Locate every Plasmodium parasite and every leukocyte.
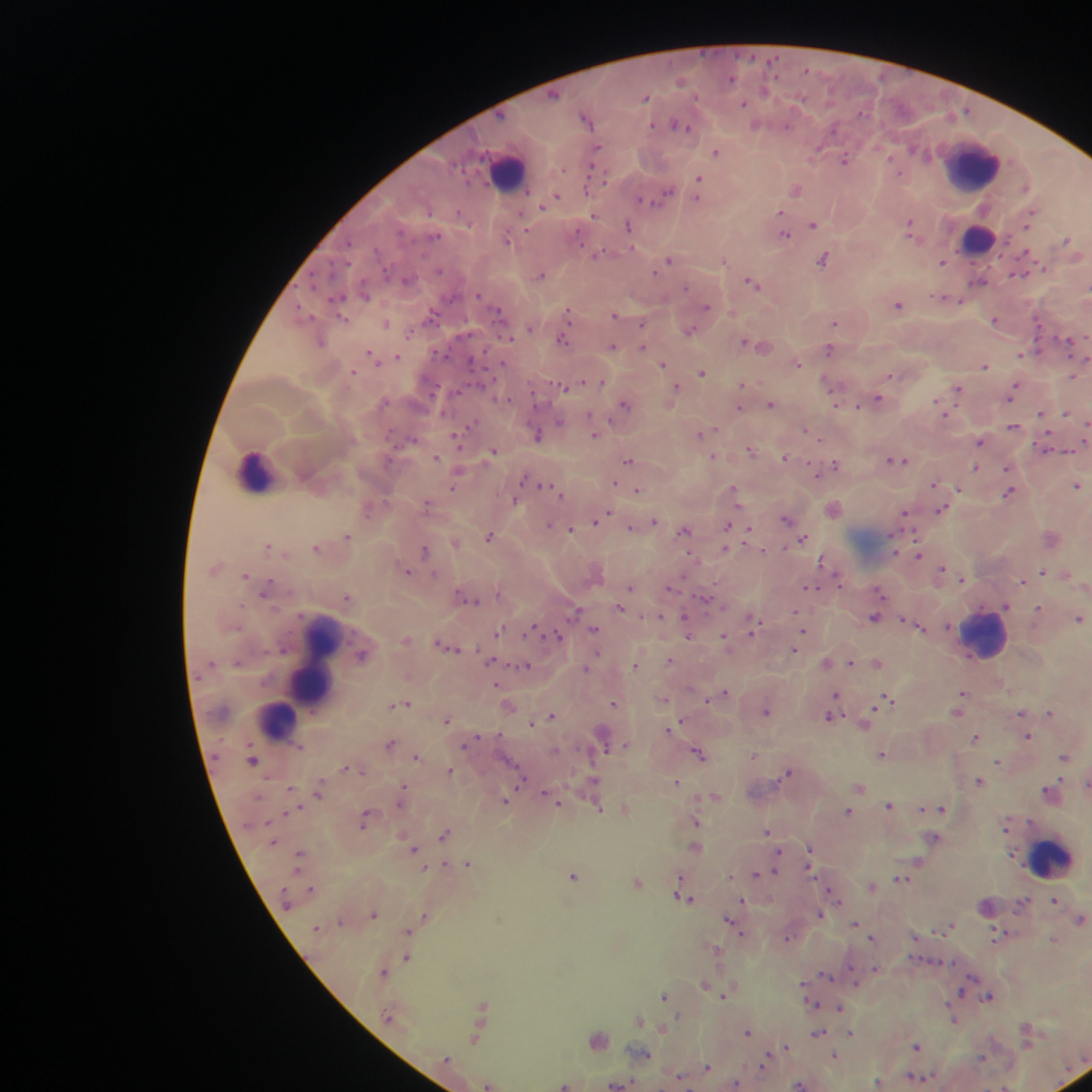
Approximate centers as (x, y) in pixels.
Plasmodium parasites: (774, 60), (807, 69), (731, 79), (680, 81), (765, 90), (554, 95), (647, 97), (802, 98), (744, 104), (863, 112), (586, 118), (680, 124), (756, 125), (652, 126), (787, 126), (833, 128), (598, 148), (915, 149), (716, 151), (816, 151), (844, 159), (899, 172), (698, 179), (1025, 187), (796, 190), (665, 194), (557, 197), (641, 199), (697, 199), (546, 203), (543, 206), (430, 211), (779, 213), (460, 214), (594, 215), (1030, 218), (813, 224), (909, 225), (1028, 225), (628, 226), (785, 234), (578, 236), (435, 237), (507, 240), (1066, 241), (349, 243), (1026, 253), (598, 254), (824, 259), (669, 261), (723, 261), (942, 262), (440, 271), (1020, 271), (653, 273), (541, 276), (407, 279), (979, 281), (753, 283), (685, 287), (364, 293), (478, 295), (941, 296), (339, 298), (960, 301), (898, 305), (707, 306), (301, 311), (569, 313), (499, 314), (614, 315), (430, 316), (344, 319), (995, 320), (835, 322), (387, 323), (642, 325), (530, 328), (689, 330), (641, 334), (510, 339), (1068, 339), (563, 340), (321, 342), (745, 342), (750, 343), (613, 346), (642, 346), (829, 350), (1021, 354), (372, 355), (398, 356), (473, 361), (663, 364), (798, 364), (984, 366), (353, 372), (702, 372), (890, 375), (1072, 376), (602, 382), (827, 382), (581, 383), (743, 384), (562, 386), (675, 386), (958, 389), (1014, 391), (878, 399), (937, 402), (624, 404), (771, 404), (858, 406), (740, 409), (1066, 413), (1041, 414), (591, 416), (560, 421), (473, 425), (1086, 425), (1014, 426), (806, 430), (702, 433), (811, 433), (595, 435), (537, 436), (412, 439), (458, 439), (980, 442), (492, 451), (751, 451), (1068, 451), (714, 456), (436, 457), (785, 457), (629, 460), (900, 460), (835, 465), (830, 468), (975, 468), (1008, 468), (815, 472), (458, 473), (525, 478), (615, 483), (935, 484), (545, 485), (1078, 486), (453, 488), (734, 488), (638, 490), (959, 490), (1009, 493), (515, 501), (427, 504), (941, 510), (905, 513), (603, 516), (598, 519), (786, 519), (655, 522), (549, 524), (728, 526), (631, 528), (571, 529), (685, 530), (748, 531), (347, 536), (489, 537), (1051, 538), (803, 539), (456, 543), (893, 544), (267, 546), (316, 548), (725, 549), (425, 551), (764, 551), (919, 555), (823, 560), (942, 570), (1042, 571), (407, 572), (245, 575), (963, 579), (1022, 581), (838, 582), (268, 587), (629, 588), (670, 588), (810, 588), (881, 593), (705, 596), (347, 597), (467, 598), (1006, 606), (621, 608), (1038, 608), (575, 610), (795, 612), (661, 616), (875, 618), (1079, 618), (948, 626), (753, 627), (920, 627), (532, 630), (594, 630), (804, 630), (499, 631), (687, 633), (558, 636), (725, 636), (407, 639), (442, 644), (450, 647), (795, 650), (362, 655), (491, 661), (669, 661), (852, 662), (877, 662), (826, 663), (635, 664), (524, 666), (587, 667), (496, 685), (724, 693), (962, 693), (835, 698), (665, 699), (707, 699), (887, 701), (960, 701), (406, 703), (613, 703), (399, 705), (509, 706), (766, 711), (957, 711), (1021, 713), (1051, 713), (551, 715), (831, 717), (447, 719), (531, 722), (866, 723), (671, 728), (1028, 737), (976, 738), (472, 741), (390, 743), (604, 745), (555, 751), (698, 753), (882, 754), (754, 755), (416, 756), (1064, 757), (253, 760), (999, 762), (348, 767), (450, 771), (788, 772), (522, 777), (676, 781), (979, 781), (594, 783), (1087, 784), (859, 787), (290, 789), (320, 790), (403, 790), (1049, 790), (547, 795), (716, 797), (505, 800), (558, 802), (889, 805), (923, 809), (942, 809), (599, 810), (848, 812), (365, 819), (695, 823), (1006, 824), (767, 831), (444, 835), (934, 839), (695, 848), (413, 849), (810, 852), (778, 854), (468, 863), (919, 863), (776, 869), (767, 873), (757, 874), (573, 876), (731, 876), (901, 879), (638, 882), (872, 886), (311, 889), (834, 896), (683, 897), (1055, 900), (743, 901), (819, 913), (373, 915), (425, 918), (1081, 919), (731, 921), (855, 923), (951, 926), (408, 931), (998, 934), (915, 936), (787, 937), (872, 938), (1054, 939), (716, 949), (408, 958), (875, 968), (383, 973), (826, 976), (705, 985), (961, 991), (725, 994), (664, 996), (989, 997), (811, 1004), (482, 1007), (839, 1009), (387, 1016), (640, 1020), (955, 1020), (663, 1027), (1027, 1028), (747, 1033), (819, 1033), (852, 1033), (475, 1039), (598, 1040), (786, 1047), (916, 1047), (643, 1053), (835, 1056), (983, 1058), (447, 1059), (765, 1062), (707, 1067), (919, 1076), (680, 1077), (736, 1083), (878, 1083), (619, 1084), (800, 1084), (489, 1085), (565, 1085), (1004, 1087).
Leukocytes: (974, 165), (508, 170), (979, 240), (256, 470), (985, 632), (317, 661), (277, 720), (1052, 858).

image size = 1092×1092 pixels
field of view = single
preparation = thick blood smear
capture = mobile-phone photograph through a microscope
country = Ghana